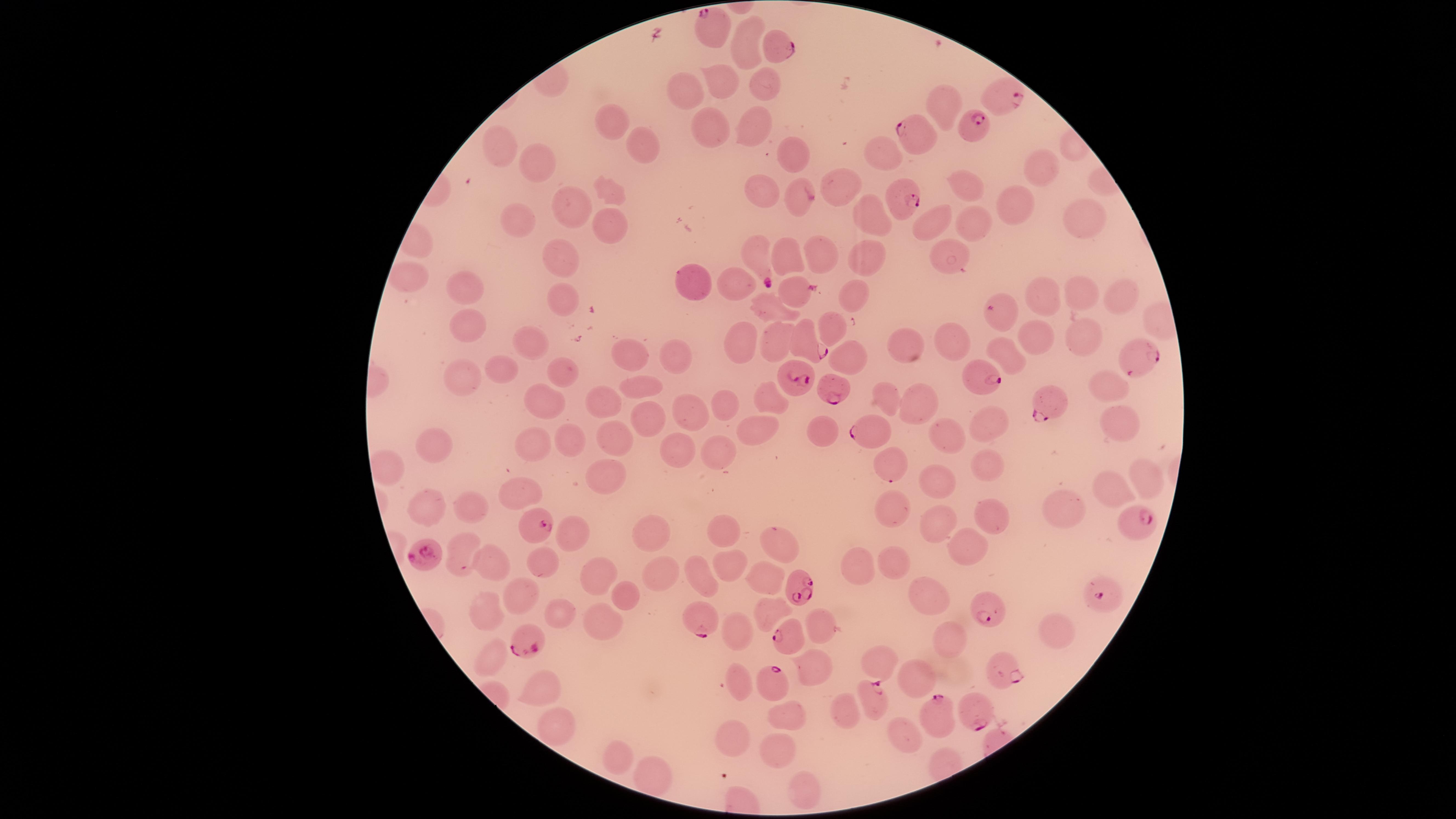 Approximate marker points as [x, y] in pixels. Parasitized RBCs: [714, 27], [775, 45], [1006, 98], [975, 126], [915, 134], [797, 198], [905, 202], [758, 253], [798, 290], [1002, 312], [806, 342], [1134, 356], [971, 375], [795, 381], [838, 388], [1047, 400], [871, 429], [1135, 522], [535, 525], [428, 551], [803, 588], [1109, 593], [992, 608], [700, 615], [520, 636], [786, 638], [1004, 670], [766, 687], [869, 697], [939, 714], [975, 714]. Uninfected RBCs: [744, 41], [715, 80], [760, 81], [690, 88], [941, 97], [609, 118], [745, 122], [707, 126], [499, 144], [883, 149], [637, 150], [789, 154], [533, 164], [1042, 171], [765, 185], [841, 187], [967, 190], [609, 192], [1016, 201], [573, 210], [873, 211], [1083, 212], [516, 223], [930, 223], [974, 223], [605, 224], [557, 252], [817, 252], [867, 253], [948, 253], [784, 256], [412, 279], [689, 282], [736, 283], [466, 284], [1116, 293], [847, 296], [1045, 296], [1083, 296], [557, 299], [770, 304], [831, 320], [469, 322], [1090, 332], [777, 333], [735, 336], [528, 340], [948, 340], [1039, 342], [907, 348], [623, 352], [672, 354], [1014, 359], [846, 360], [493, 368], [463, 371], [554, 371], [646, 382], [1102, 383], [767, 394], [545, 401], [602, 402], [888, 402], [696, 405], [913, 408], [724, 409], [1120, 409], [647, 417], [988, 419], [753, 427], [822, 427], [950, 435], [610, 439], [440, 440], [573, 441], [677, 442], [528, 449], [716, 451], [895, 455], [990, 458], [394, 463], [601, 473], [1143, 474], [946, 477], [1113, 490], [513, 495], [425, 502], [467, 504], [891, 506], [1066, 510], [989, 514], [935, 520], [723, 529], [574, 531], [655, 535], [776, 542], [965, 547], [463, 557], [482, 562], [545, 563], [728, 563], [861, 564], [895, 567], [593, 569], [665, 570], [763, 573], [703, 575], [922, 592], [519, 594], [623, 594], [491, 606], [768, 608], [562, 614], [818, 619], [599, 622], [950, 631], [1057, 631], [743, 637], [494, 654], [819, 658], [883, 660], [913, 676], [540, 686], [739, 686], [848, 711], [792, 715], [553, 720], [899, 730], [736, 732], [780, 747], [615, 754], [650, 778], [800, 785]. Single field of view. Circular visible region. Species: Plasmodium falciparum. Thin blood film. Presence: malaria parasites seen. Giemsa-stained preparation. Photographed with a smartphone camera through the microscope eyepiece. Image is 1456×819 pixels.